Classify the preparation.
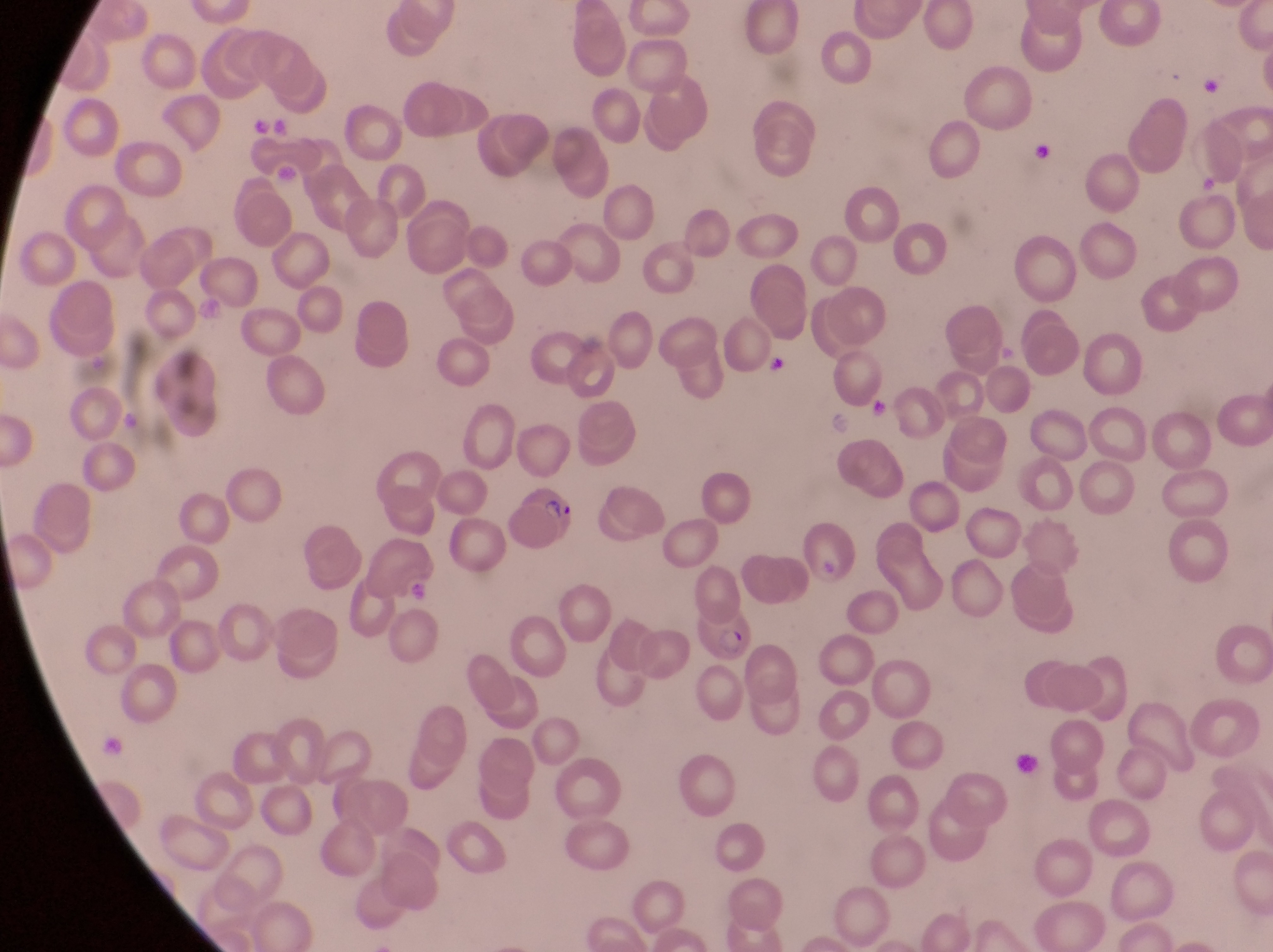

Thin blood smear.

Approximate bounding boxes as left top right bottom in pixels. Parasitised red blood cell locations: 504 489 582 554; 689 599 754 669. Artifact (platelet-like body, stain precipitate, or debris) locations: 1202 74 1225 97; 244 115 277 142; 1035 140 1056 168; 768 356 791 379; 871 398 894 424; 405 574 433 606; 1014 746 1046 781. Photographed through the eyepiece of an Olympus CX-23 microscope with a smartphone camera. Single field of view. Image is 1273×952 pixels. Magnification of 1000x. Collected in Uganda.